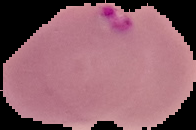
Summary:
  - Image size: 196×130 pixels
  - Preparation: thin blood smear
  - Image type: segmented cell region with the area outside set to black
  - Result: Plasmodium parasites detected